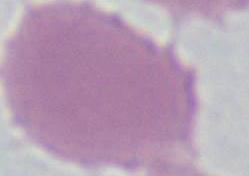

An erythrocyte is seen. 1000x magnification. Micrograph.